State the preparation type.
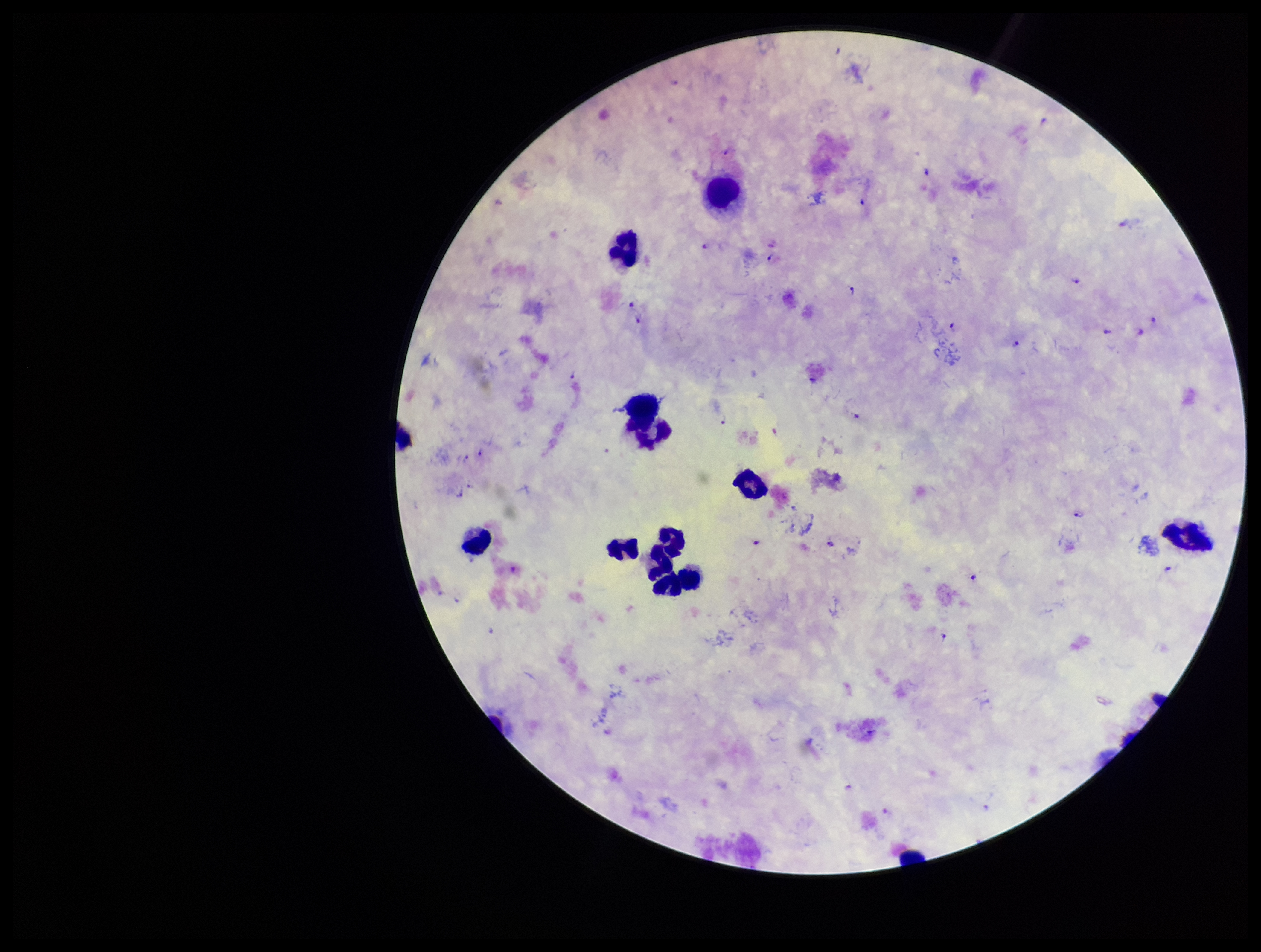
Thick.

Photographed through the microscope eyepiece with a smartphone camera. Patient malaria status: positive. Plasmodium parasites: identified. Parasite count: 27. Stained with Giemsa. Image is 1261×952 pixels. Species reported for this patient: Plasmodium falciparum. Single field of view. Leukocyte count: 11.